Give the position of every Plasmodium parasite.
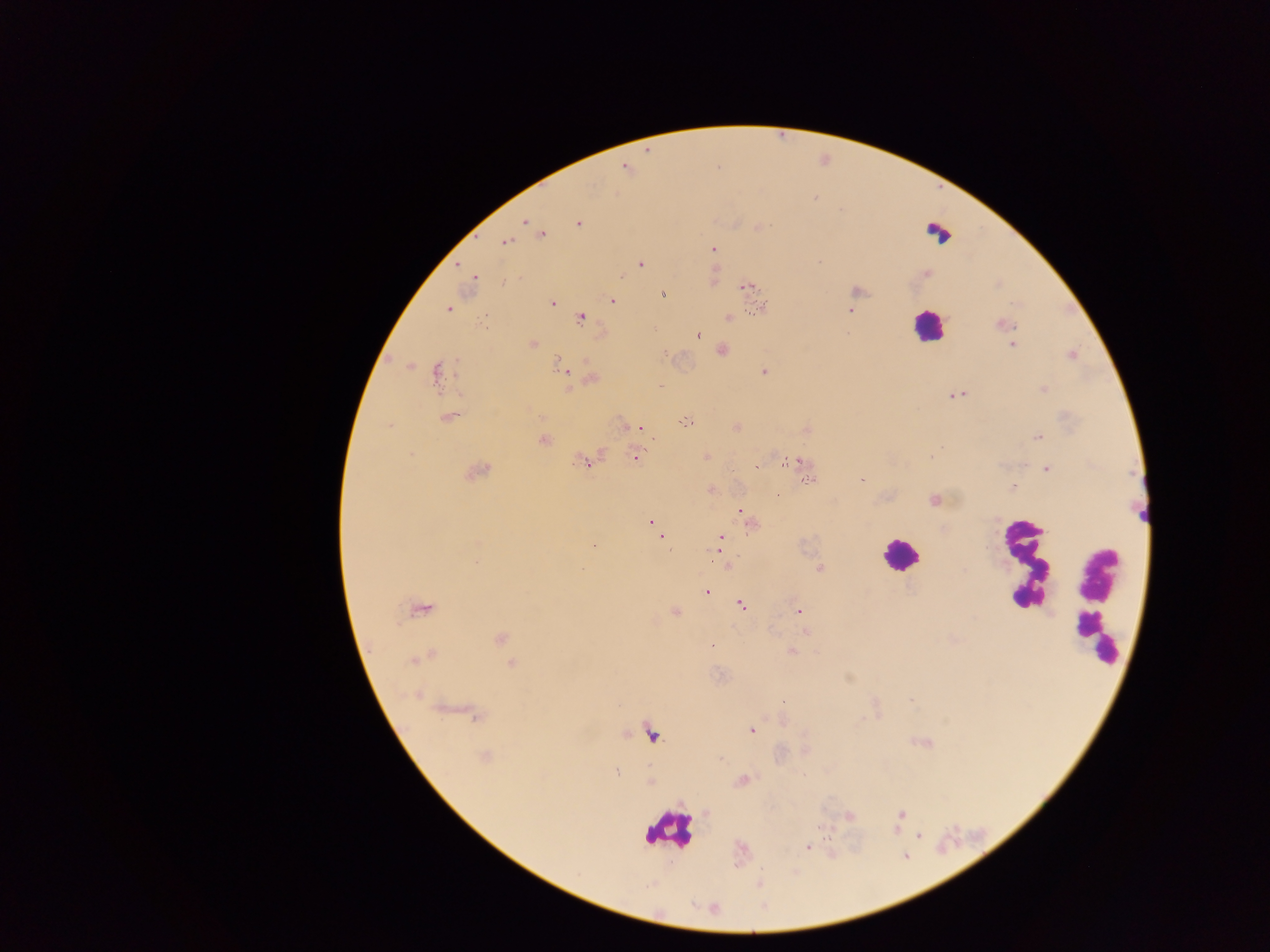
Approximate centers as [x, y] in pixels.
Plasmodium parasites: [626, 167], [525, 221], [578, 222], [538, 232], [540, 235], [505, 241], [712, 249], [639, 263], [458, 265], [926, 274], [713, 275], [474, 279], [745, 287], [855, 290], [661, 295], [612, 300], [551, 302], [761, 307], [448, 309], [851, 311], [580, 316], [728, 317], [1002, 324], [698, 335], [532, 344], [1012, 344], [721, 350], [1071, 354], [409, 365], [562, 365], [763, 371], [438, 372], [591, 378], [568, 388], [1043, 390], [957, 394], [448, 416], [685, 421], [638, 427], [735, 427], [807, 430], [1037, 437], [542, 439], [706, 456], [636, 457], [586, 460], [792, 461], [757, 466], [801, 467], [1046, 469], [476, 470], [807, 479], [860, 479], [1012, 486], [711, 489], [777, 495], [934, 500], [741, 509], [651, 521], [750, 525], [659, 529], [660, 535], [720, 538], [593, 545], [718, 548], [727, 565], [820, 568], [707, 591], [741, 604], [421, 607], [798, 611], [675, 612], [805, 631], [500, 638], [711, 645], [791, 652], [421, 657], [512, 664], [417, 694], [474, 714], [751, 730], [652, 733], [920, 741], [485, 757], [615, 772], [742, 780], [650, 781], [899, 814], [848, 816], [918, 834], [808, 846].

preparation = thick blood smear
field of view = single
capture = mobile-phone photograph through a microscope
image size = 1270×952 pixels
country = Ghana
leukocyte locations = approximate centers as [x, y] in pixels: [937, 233], [927, 326], [900, 555], [1025, 563], [1098, 601], [668, 829]